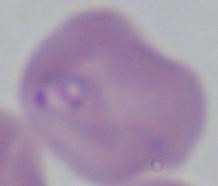 1000x magnification. Micrograph. A Babesia parasite is seen.